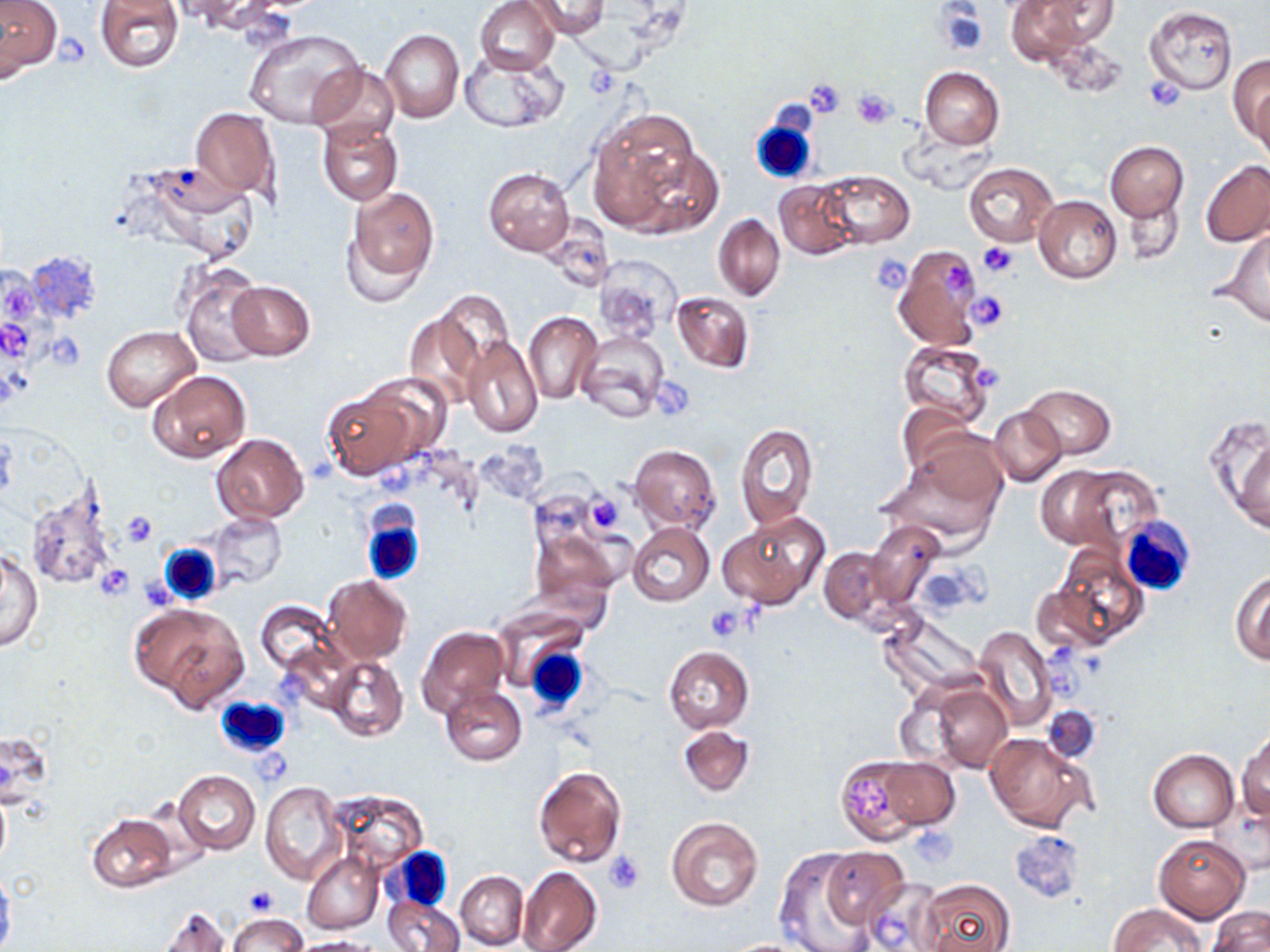
Approximate bounding boxes as named x1/y1/x2/y2 corners in pixels. Uninfected red blood cell locations: (x1=475, y1=0, x2=560, y2=75), (x1=524, y1=0, x2=610, y2=39), (x1=1004, y1=0, x2=1095, y2=66), (x1=1037, y1=1, x2=1120, y2=46), (x1=0, y1=2, x2=62, y2=79), (x1=94, y1=2, x2=183, y2=71), (x1=1144, y1=6, x2=1238, y2=95), (x1=245, y1=28, x2=365, y2=128), (x1=379, y1=29, x2=464, y2=123), (x1=461, y1=51, x2=566, y2=132), (x1=1228, y1=55, x2=1270, y2=149), (x1=308, y1=64, x2=400, y2=146), (x1=919, y1=67, x2=1004, y2=148), (x1=1248, y1=81, x2=1269, y2=165), (x1=190, y1=108, x2=279, y2=199), (x1=588, y1=112, x2=707, y2=233), (x1=317, y1=119, x2=403, y2=206), (x1=1106, y1=142, x2=1188, y2=220), (x1=626, y1=145, x2=723, y2=237), (x1=1201, y1=160, x2=1270, y2=247), (x1=135, y1=161, x2=260, y2=261), (x1=962, y1=161, x2=1059, y2=246), (x1=483, y1=168, x2=574, y2=255), (x1=819, y1=170, x2=914, y2=247), (x1=773, y1=179, x2=859, y2=259), (x1=341, y1=184, x2=439, y2=300), (x1=1125, y1=192, x2=1185, y2=265), (x1=1034, y1=196, x2=1122, y2=283), (x1=713, y1=214, x2=785, y2=301), (x1=540, y1=216, x2=615, y2=293), (x1=1221, y1=230, x2=1270, y2=325), (x1=892, y1=245, x2=985, y2=352), (x1=593, y1=255, x2=679, y2=339), (x1=176, y1=264, x2=264, y2=366), (x1=227, y1=279, x2=314, y2=360), (x1=431, y1=290, x2=516, y2=384), (x1=671, y1=290, x2=754, y2=374), (x1=401, y1=305, x2=490, y2=411), (x1=523, y1=311, x2=602, y2=403), (x1=103, y1=327, x2=200, y2=411), (x1=576, y1=329, x2=670, y2=422), (x1=461, y1=333, x2=543, y2=438), (x1=898, y1=340, x2=996, y2=427), (x1=148, y1=369, x2=252, y2=463), (x1=366, y1=373, x2=453, y2=459), (x1=1022, y1=384, x2=1116, y2=459), (x1=321, y1=387, x2=421, y2=478), (x1=896, y1=401, x2=973, y2=478), (x1=989, y1=407, x2=1067, y2=487), (x1=1209, y1=415, x2=1270, y2=538), (x1=735, y1=423, x2=818, y2=528), (x1=212, y1=433, x2=310, y2=524), (x1=628, y1=444, x2=721, y2=533), (x1=881, y1=445, x2=1007, y2=548), (x1=1039, y1=467, x2=1154, y2=551), (x1=21, y1=482, x2=122, y2=592), (x1=206, y1=513, x2=287, y2=591), (x1=718, y1=514, x2=827, y2=610), (x1=866, y1=518, x2=947, y2=609), (x1=628, y1=522, x2=714, y2=606), (x1=529, y1=523, x2=623, y2=609), (x1=1050, y1=543, x2=1148, y2=647), (x1=819, y1=547, x2=890, y2=625), (x1=1, y1=551, x2=42, y2=652), (x1=916, y1=565, x2=983, y2=614), (x1=1230, y1=571, x2=1270, y2=665), (x1=323, y1=574, x2=411, y2=663), (x1=254, y1=601, x2=340, y2=680), (x1=134, y1=603, x2=249, y2=710), (x1=878, y1=613, x2=983, y2=698), (x1=417, y1=625, x2=511, y2=719), (x1=972, y1=625, x2=1058, y2=730), (x1=665, y1=646, x2=754, y2=732), (x1=326, y1=655, x2=407, y2=740), (x1=921, y1=681, x2=1013, y2=773), (x1=440, y1=685, x2=527, y2=766), (x1=1043, y1=706, x2=1101, y2=760), (x1=677, y1=722, x2=756, y2=797), (x1=1238, y1=729, x2=1270, y2=821), (x1=984, y1=732, x2=1094, y2=832), (x1=1149, y1=749, x2=1239, y2=832), (x1=835, y1=755, x2=931, y2=844), (x1=873, y1=755, x2=959, y2=832), (x1=533, y1=765, x2=627, y2=867), (x1=173, y1=770, x2=260, y2=854), (x1=261, y1=782, x2=345, y2=884), (x1=0, y1=788, x2=11, y2=869), (x1=329, y1=790, x2=428, y2=871), (x1=87, y1=815, x2=178, y2=892), (x1=666, y1=817, x2=764, y2=912), (x1=1153, y1=834, x2=1249, y2=922), (x1=772, y1=847, x2=876, y2=952), (x1=820, y1=847, x2=909, y2=930), (x1=303, y1=851, x2=383, y2=934), (x1=518, y1=867, x2=602, y2=952), (x1=0, y1=870, x2=15, y2=950), (x1=456, y1=871, x2=528, y2=950), (x1=917, y1=877, x2=1016, y2=952), (x1=857, y1=878, x2=947, y2=952), (x1=383, y1=894, x2=464, y2=952), (x1=1107, y1=903, x2=1206, y2=951), (x1=153, y1=906, x2=231, y2=952), (x1=1207, y1=906, x2=1270, y2=952), (x1=229, y1=915, x2=304, y2=951), (x1=291, y1=936, x2=382, y2=952), (x1=715, y1=938, x2=826, y2=951). White blood cell locations: (x1=752, y1=115, x2=817, y2=181), (x1=360, y1=509, x2=427, y2=586), (x1=1117, y1=516, x2=1195, y2=598), (x1=160, y1=545, x2=220, y2=605), (x1=521, y1=643, x2=590, y2=716), (x1=215, y1=696, x2=289, y2=758), (x1=387, y1=848, x2=455, y2=912). Platelet locations: (x1=55, y1=34, x2=91, y2=66), (x1=1145, y1=77, x2=1184, y2=113), (x1=803, y1=78, x2=847, y2=118), (x1=851, y1=90, x2=897, y2=129), (x1=977, y1=241, x2=1020, y2=278), (x1=870, y1=253, x2=913, y2=292), (x1=945, y1=262, x2=972, y2=293), (x1=966, y1=292, x2=1010, y2=331), (x1=46, y1=332, x2=88, y2=371), (x1=974, y1=365, x2=1002, y2=387), (x1=654, y1=380, x2=692, y2=421), (x1=584, y1=494, x2=625, y2=534), (x1=119, y1=509, x2=159, y2=548), (x1=95, y1=565, x2=134, y2=601), (x1=138, y1=574, x2=180, y2=609), (x1=705, y1=607, x2=748, y2=641), (x1=850, y1=778, x2=894, y2=821), (x1=911, y1=828, x2=958, y2=868), (x1=1011, y1=828, x2=1085, y2=901), (x1=604, y1=850, x2=644, y2=893), (x1=241, y1=884, x2=276, y2=915). Slide-level diagnosis: negative for blood parasites. Single field of view. Thin blood smear. 1000x magnification. Image is 1270×952 pixels. May-Grünwald-Giemsa-stained preparation. Light microscopy.